State which cell type is depicted.
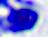

This is a leukocyte.

Summary:
  - Modality: photomicrograph
  - Magnification: 400x